Outline each blood parasite and name the species.
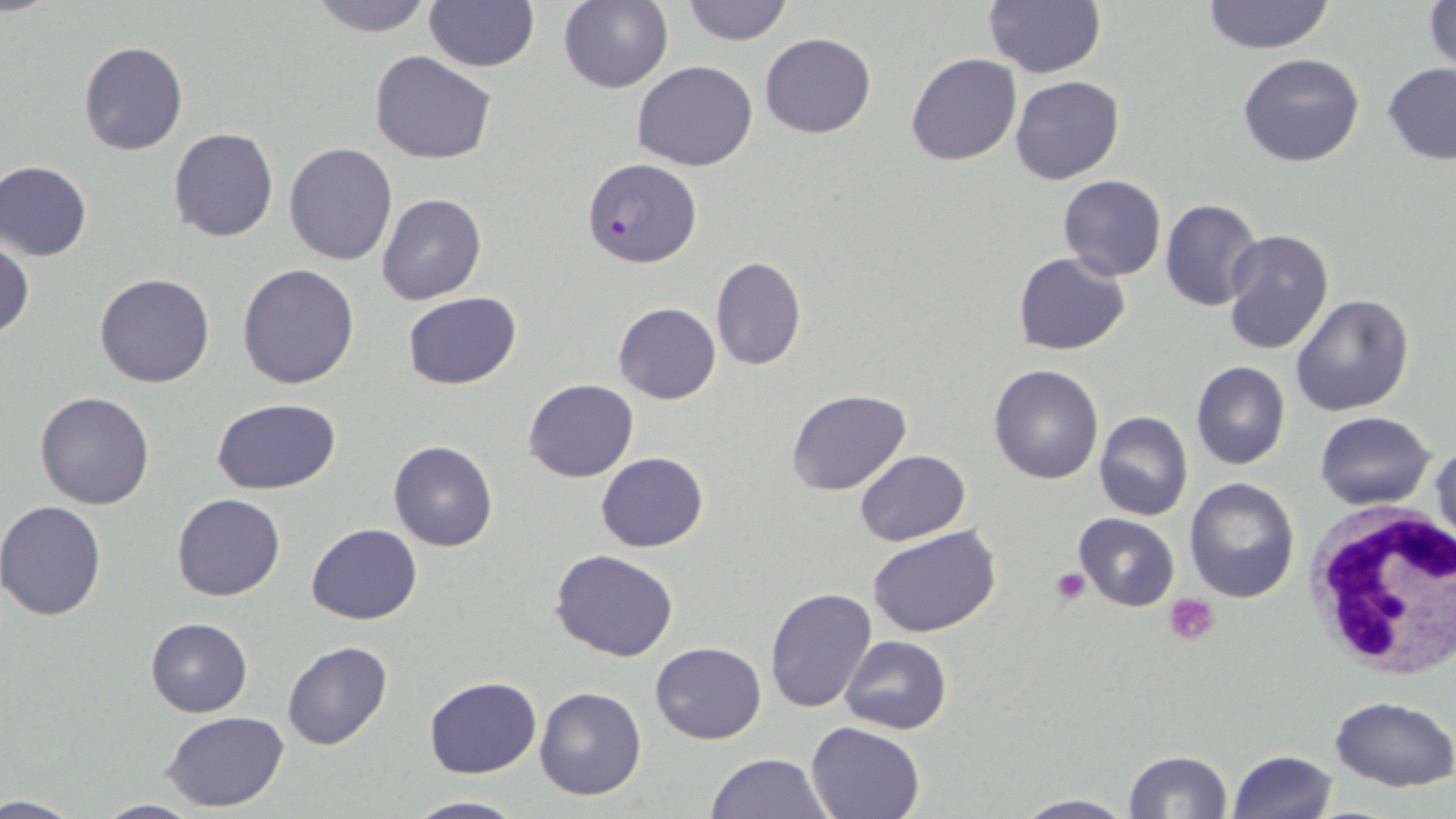

Approximate bounding boxes as (x1,y1)-(x2,y2) corner pairs in pixels.
Plasmodium falciparum-infected red blood cells: (582,158)-(703,268).
No Plasmodium ovale, Plasmodium malariae, Plasmodium vivax, Babesia divergens, or Trypanosoma brucei observed.

White blood cell locations: (1303,503)-(1456,673). Platelet locations: (1052,569)-(1089,605), (1165,594)-(1220,645). Uninfected red blood cell locations: (305,0)-(437,37), (558,0)-(673,93), (679,0)-(796,46), (982,0)-(1107,78), (1200,0)-(1337,54), (425,1)-(539,72), (1423,1)-(1455,76), (760,33)-(876,138), (77,40)-(187,157), (369,51)-(497,164), (905,52)-(1022,166), (1237,52)-(1366,167), (632,60)-(758,170), (1381,62)-(1456,164), (1009,75)-(1125,184), (168,128)-(279,243), (283,144)-(397,264), (1,160)-(92,261), (1057,175)-(1166,281), (377,195)-(487,306), (1160,199)-(1264,311), (1223,229)-(1334,356), (0,239)-(33,340), (1014,252)-(1130,354), (710,256)-(807,371), (237,264)-(360,389), (95,273)-(215,388), (402,291)-(522,389), (1290,293)-(1413,416), (614,303)-(720,405), (1191,360)-(1290,470), (989,363)-(1104,484), (523,378)-(638,483), (786,388)-(911,495), (35,391)-(155,510), (210,397)-(342,494), (1095,412)-(1193,522), (1316,412)-(1435,509), (1430,439)-(1455,558), (388,441)-(498,552), (855,449)-(970,545), (596,452)-(708,550), (1185,478)-(1299,603), (171,493)-(285,601), (0,501)-(108,619), (1073,513)-(1179,612), (306,523)-(421,625), (869,526)-(1001,638), (549,549)-(679,662), (765,587)-(879,715), (146,618)-(252,716), (841,635)-(951,734), (282,641)-(394,751), (650,641)-(767,744), (424,676)-(542,778), (534,685)-(647,801), (1329,696)-(1456,791), (162,711)-(291,812), (806,721)-(926,818), (1122,749)-(1233,818), (1227,749)-(1339,819), (704,753)-(834,818), (0,793)-(89,817), (1014,793)-(1135,818), (403,794)-(527,818), (88,798)-(206,818). Slide-level diagnosis: Plasmodium falciparum. Single field of view. Thin blood film. May-Grünwald-Giemsa-stained preparation. Captured at 1000x magnification. Image is 1456×819 pixels. Light microscopy.